Describe the morphology of the erythrocytes.
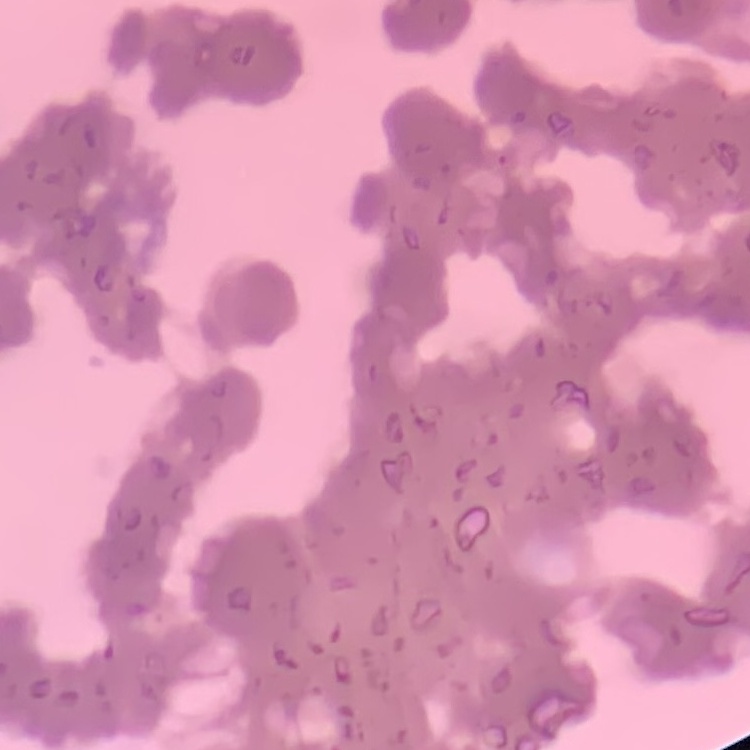
They show rouleaux formation.

One tile cut from a larger photomicrograph. Field's or Giemsa stain. Thin blood smear.